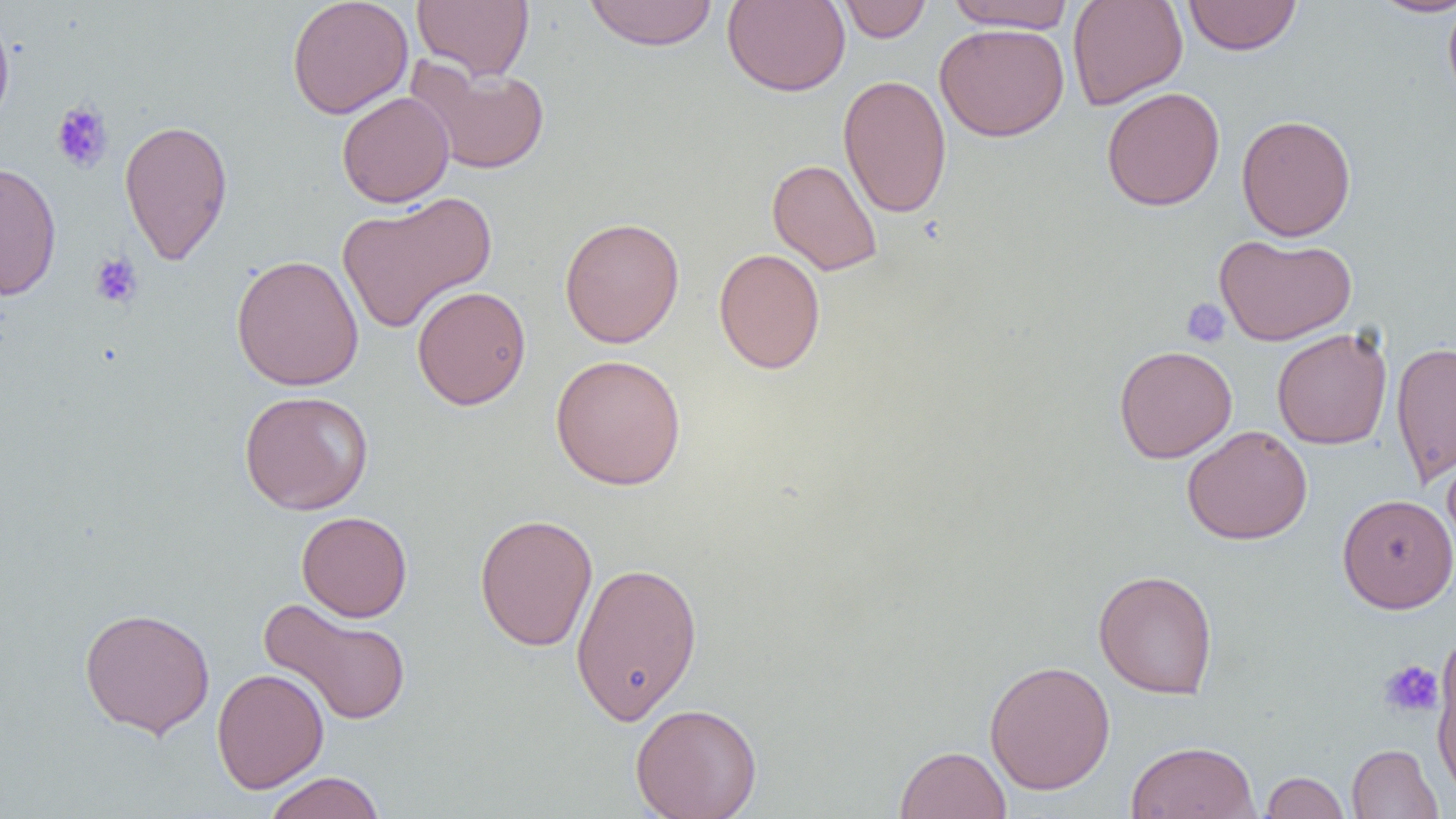

Summary:
  - Coordinate format: approximate bounding boxes as [x1, y1, x2, y2] in pixels
  - Platelet locations: [50, 101, 113, 173], [90, 252, 143, 309], [1181, 298, 1230, 347], [1378, 660, 1443, 720]
  - Uninfected red blood cell locations: [286, 0, 413, 119], [412, 0, 534, 81], [583, 0, 719, 50], [721, 0, 850, 97], [837, 0, 932, 42], [1067, 0, 1187, 110], [1182, 0, 1303, 56], [1367, 0, 1456, 17], [1443, 0, 1456, 108], [942, 1, 1077, 32], [0, 10, 15, 135], [934, 23, 1070, 142], [405, 59, 550, 175], [838, 74, 953, 218], [1101, 87, 1225, 211], [336, 91, 454, 208], [1236, 114, 1356, 241], [118, 118, 234, 265], [767, 158, 883, 276], [0, 161, 62, 302], [336, 192, 497, 334], [559, 217, 685, 348], [1214, 234, 1357, 346], [714, 248, 826, 374], [231, 254, 364, 391], [412, 285, 530, 410], [1271, 327, 1392, 450], [1390, 341, 1456, 487], [1113, 344, 1238, 463], [549, 354, 687, 490], [239, 390, 374, 515], [1182, 425, 1312, 545], [1443, 446, 1456, 562], [1337, 493, 1456, 614], [296, 510, 412, 622], [474, 513, 598, 652], [570, 560, 703, 725], [1093, 569, 1218, 698], [258, 596, 412, 727], [79, 606, 216, 738], [1432, 640, 1455, 796], [984, 659, 1115, 795], [211, 668, 329, 793], [630, 702, 763, 818], [1125, 740, 1261, 819], [1346, 743, 1443, 819], [894, 745, 1012, 819], [262, 771, 387, 819], [1260, 771, 1350, 818]
  - Slide-level diagnosis: no evidence of blood parasites
  - Modality: light microscopy
  - Magnification: 1000x
  - Preparation: thin blood smear
  - Field of view: one of a larger specimen
  - Image size: 1456×819 pixels